Assess this cell for malaria.
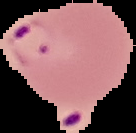

It is parasitized.

Image is 136×133 pixels. From a thin blood film. Segmented cell region on a black background.